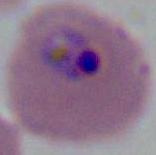
modality: micrograph
magnification: 400x or 1000x
identification: Plasmodium